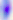

{
  "magnification": "400x",
  "identification": "Toxoplasma gondii",
  "modality": "micrograph"
}